State which cell type is depicted.
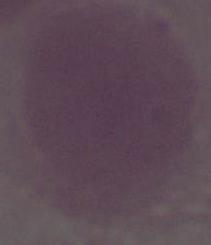

This is an erythrocyte.

Captured at 1000x magnification. Photomicrograph.